Point out each Plasmodium parasite.
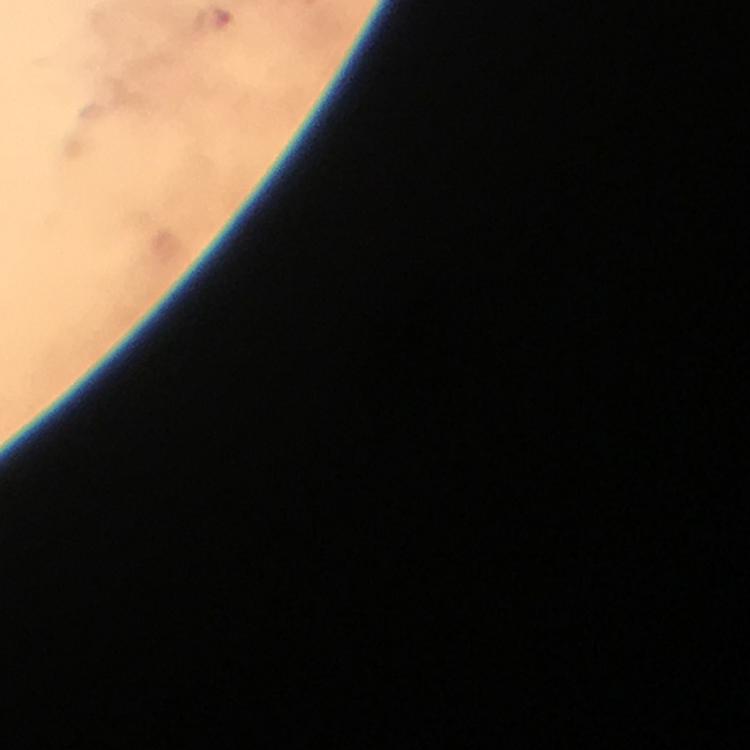

Approximate centers as [x, y] in pixels.
Plasmodium parasites: [212, 20].

Immersion oil applied. Thick blood smear. Image is 750×750 pixels. Giemsa stain. From a diagnostic examination for malaria. A crop from one field of view. 100x magnification. Smartphone photograph taken through a microscope.